Assess this cell for malaria.
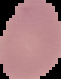

It is uninfected.

Image is 61×79 pixels. Segmented cell region on a black background. From a thin blood smear.